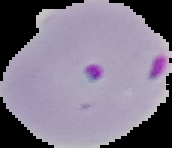
Image is 172×148 pixels. Result: Plasmodium parasites detected. From a thin blood smear. Segmented cell region on a black background.